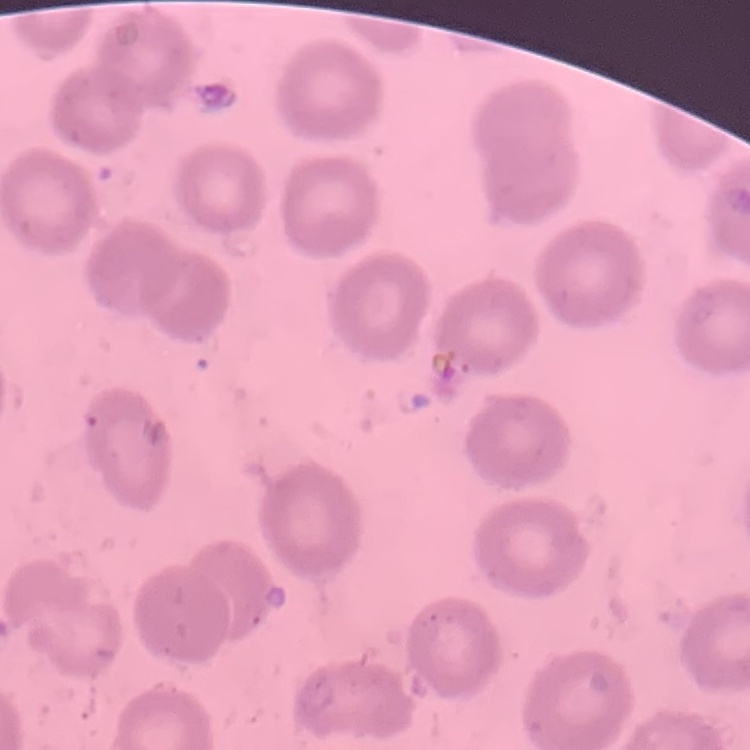

The red blood cells exhibit no rouleaux formation. Thin blood film. Square crop of a larger photomicrograph. Stained with either Field's or Giemsa.